Report the malaria status of this cell.
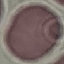
Uninfected.

Photographed with a smartphone camera at the microscope eyepiece. Thin blood smear. Cell patch, automatically extracted from a larger field of view and resized to 64 × 64 pixels. Giemsa-stained preparation.